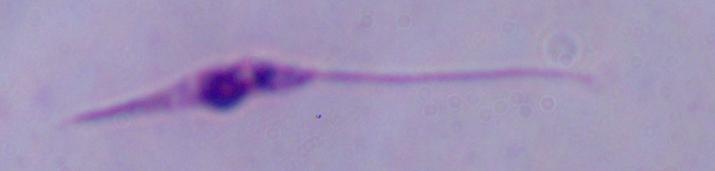
Photomicrograph. A Leishmania parasite is seen. 1000x magnification.